Report the malaria status of this cell.
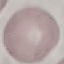
Uninfected.

capture = smartphone through the microscope eyepiece
stain = Giemsa
preparation = thin blood smear
image type = cell patch, automatically extracted from a larger field of view and resized to 64 × 64 pixels